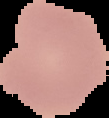

{
  "malaria_status": "uninfected",
  "preparation": "thin blood film",
  "image_type": "cell region segmented out of the field of view; surrounding area masked to black",
  "image_size": "109×118 pixels"
}